Outline every malaria parasite, every leukocyte, and every artifact (stain precipitate or debris).
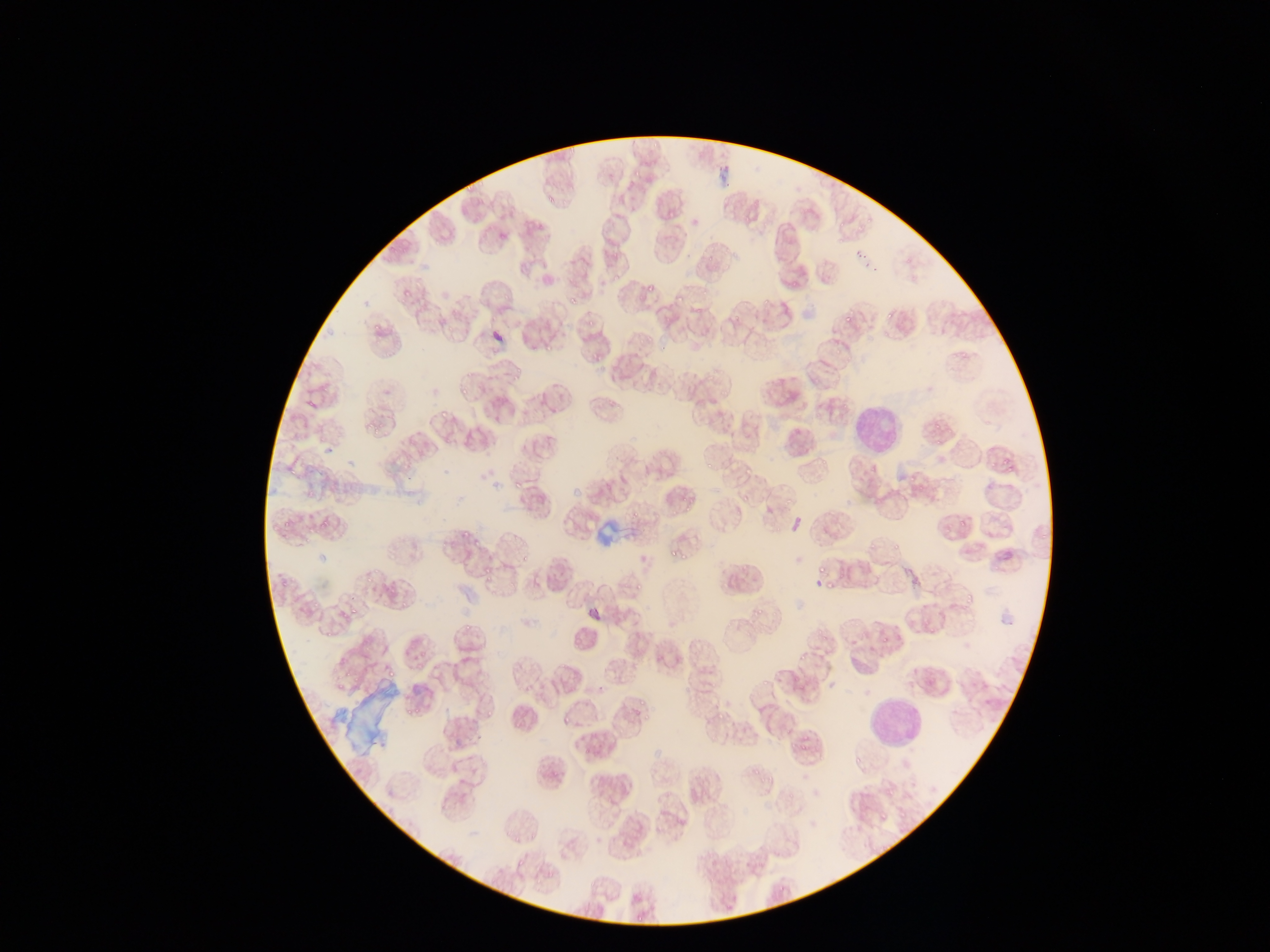
Approximate bounding boxes as {left, top, right, bottom} in pixels.
Malaria parasites: {463, 175, 476, 196}, {538, 193, 555, 208}, {610, 273, 622, 282}, {788, 278, 797, 286}, {643, 284, 656, 293}, {398, 285, 412, 303}, {570, 288, 579, 307}, {673, 295, 686, 304}, {764, 295, 770, 303}, {731, 310, 742, 323}, {840, 310, 847, 323}, {881, 312, 891, 325}, {371, 313, 381, 332}, {586, 315, 592, 324}, {541, 340, 553, 357}, {589, 347, 609, 364}, {955, 352, 969, 361}, {512, 365, 522, 379}, {459, 382, 471, 396}, {306, 393, 316, 408}, {438, 405, 448, 422}, {363, 421, 376, 436}, {933, 422, 942, 431}, {936, 437, 945, 444}, {983, 450, 1002, 473}, {1004, 455, 1019, 472}, {703, 459, 714, 473}, {286, 461, 297, 478}, {512, 470, 528, 491}, {909, 471, 922, 481}, {306, 487, 318, 498}, {785, 491, 796, 504}, {738, 495, 756, 507}, {682, 501, 693, 511}, {629, 507, 643, 520}, {953, 507, 974, 526}, {278, 509, 300, 535}, {315, 512, 336, 535}, {461, 526, 470, 539}, {865, 529, 886, 553}, {889, 537, 904, 551}, {469, 541, 483, 549}, {668, 544, 679, 557}, {675, 546, 690, 561}, {519, 556, 529, 567}, {483, 561, 489, 581}, {816, 568, 828, 578}, {282, 574, 300, 590}, {364, 575, 373, 585}, {388, 577, 398, 594}, {510, 577, 514, 588}, {964, 577, 977, 604}, {826, 579, 836, 588}, {843, 579, 861, 589}, {635, 581, 642, 593}, {310, 589, 326, 611}, {747, 603, 769, 617}, {337, 609, 346, 624}, {352, 611, 359, 620}, {327, 623, 340, 638}, {461, 623, 471, 636}, {881, 635, 894, 644}, {799, 650, 814, 662}, {413, 658, 430, 667}, {391, 666, 396, 679}, {757, 676, 770, 689}, {637, 691, 653, 709}, {633, 704, 646, 718}, {486, 707, 500, 718}, {716, 712, 725, 726}, {563, 715, 573, 727}, {801, 726, 821, 739}, {802, 742, 817, 752}, {751, 764, 759, 777}, {894, 806, 913, 827} | approximate {x, y} pixel centers of objects too small to bound: {746, 470}, {403, 609}.
Leukocytes: {848, 395, 908, 461}, {396, 675, 440, 717}, {864, 693, 924, 753}.
Artifacts (stain precipitate or debris): {589, 513, 625, 547}.

country = Ghana
preparation = thin blood smear
capture = mobile-phone photograph through a microscope
field of view = single
image size = 1270×952 pixels